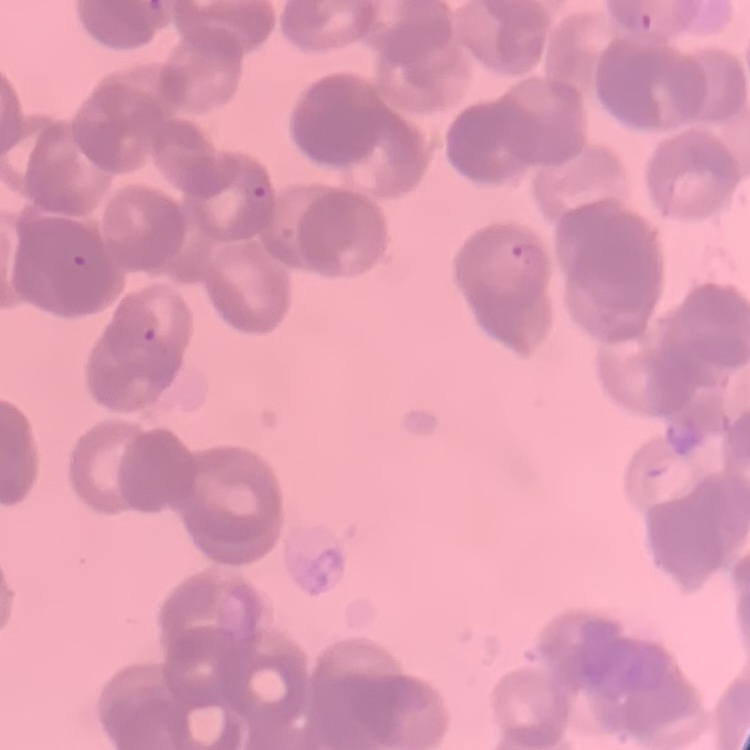

Summary:
  - Erythrocyte morphology: rouleaux formation
  - Preparation: thin peripheral smear
  - Image type: one tile cut from a larger photomicrograph
  - Stain: Field's or Giemsa